Locate every parasitized red blood cell.
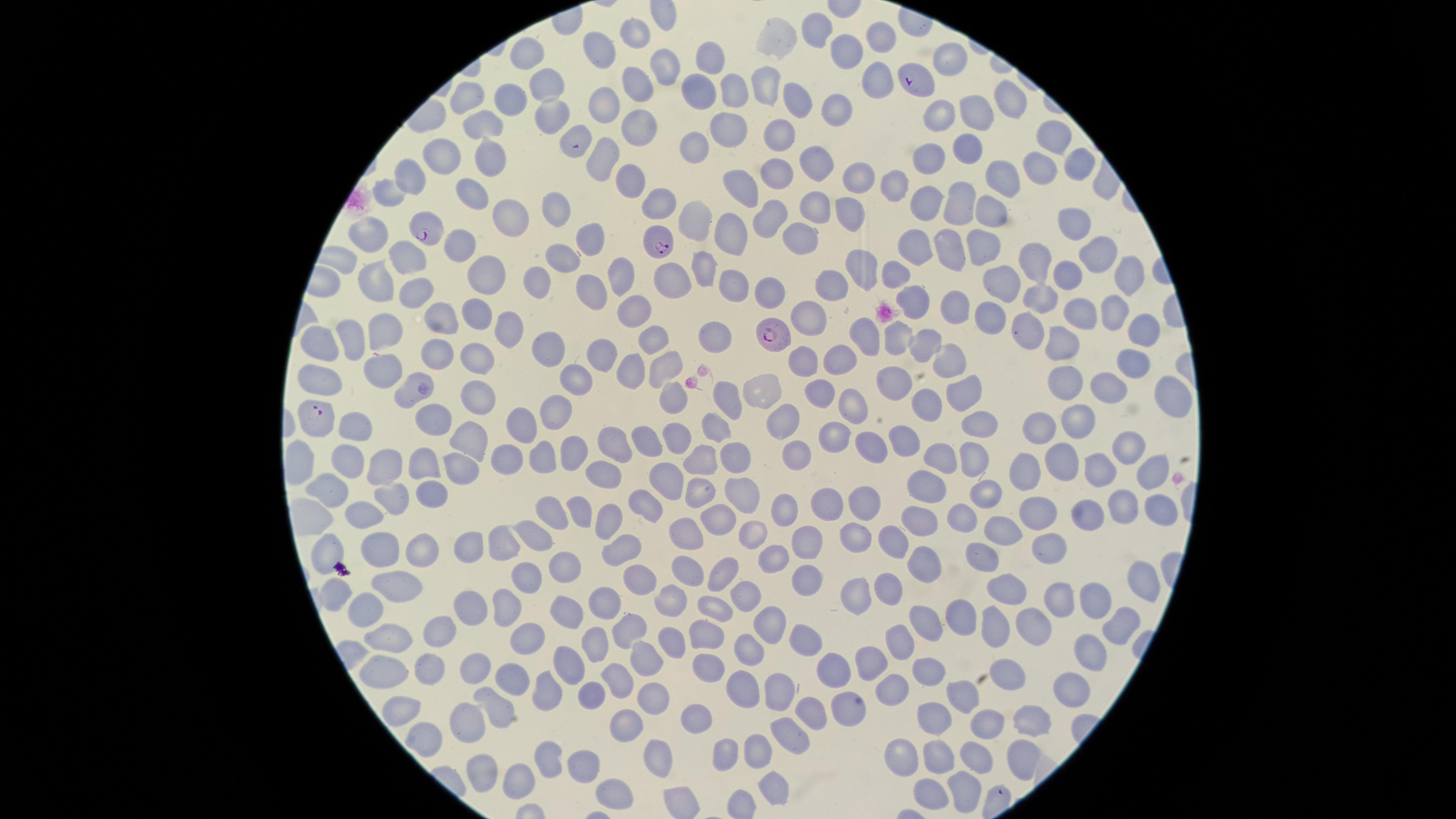

Approximate marker points as {x, y} in pixels.
Parasitized red blood cells: {914, 81}, {426, 230}, {662, 242}, {776, 335}, {314, 416}.

{
  "species": "Plasmodium falciparum",
  "uninfected_red_blood_cells": "approximate marker points as {x, y} in pixels: {823, 26}, {641, 33}, {881, 34}, {776, 39}, {848, 49}, {523, 53}, {603, 54}, {952, 57}, {708, 59}, {658, 69}, {874, 75}, {541, 78}, {766, 79}, {633, 85}, {705, 88}, {732, 91}, {467, 97}, {509, 98}, {1002, 100}, {804, 101}, {836, 101}, {606, 104}, {969, 111}, {545, 112}, {938, 114}, {479, 121}, {731, 121}, {634, 122}, {580, 129}, {1054, 133}, {778, 134}, {701, 143}, {442, 149}, {971, 150}, {486, 153}, {603, 155}, {1075, 159}, {931, 160}, {1039, 164}, {823, 166}, {410, 171}, {780, 173}, {1008, 175}, {862, 181}, {628, 182}, {898, 184}, {745, 188}, {387, 193}, {468, 196}, {652, 200}, {925, 200}, {958, 202}, {816, 203}, {985, 205}, {555, 209}, {769, 213}, {845, 213}, {505, 217}, {699, 219}, {1068, 221}, {372, 230}, {734, 231}, {587, 238}, {808, 238}, {460, 243}, {922, 244}, {986, 245}, {1099, 248}, {958, 249}, {1041, 255}, {408, 257}, {561, 257}, {865, 263}, {484, 266}, {705, 266}, {897, 270}, {1063, 272}, {539, 273}, {1122, 273}, {626, 274}, {673, 277}, {372, 278}, {839, 279}, {1005, 280}, {733, 283}, {769, 291}, {414, 293}, {593, 293}, {1041, 297}, {919, 302}, {961, 302}, {1112, 309}, {1085, 310}, {640, 311}, {440, 313}, {471, 314}, {810, 315}, {993, 316}, {499, 325}, {1026, 326}, {1140, 326}, {387, 332}, {351, 334}, {871, 334}, {716, 335}, {897, 337}, {321, 338}, {654, 340}, {929, 340}, {1066, 341}, {475, 352}, {596, 352}, {547, 353}, {837, 355}, {436, 356}, {953, 356}, {1136, 359}, {665, 363}, {376, 371}, {637, 371}, {316, 376}, {580, 376}, {893, 376}, {1066, 379}, {1108, 381}, {758, 386}, {408, 390}, {820, 391}, {967, 391}, {664, 392}, {1177, 392}, {724, 395}, {468, 400}, {924, 401}, {557, 403}, {853, 403}, {984, 416}, {426, 417}, {520, 419}, {781, 420}, {1075, 420}, {1045, 422}, {717, 426}, {361, 428}, {835, 434}, {651, 438}, {910, 439}, {679, 442}, {473, 443}, {865, 443}, {1126, 443}, {610, 445}, {795, 450}, {569, 453}, {732, 455}, {1056, 455}, {539, 457}, {351, 458}, {506, 458}, {948, 458}, {702, 459}, {972, 459}, {385, 465}, {426, 465}, {463, 469}, {1102, 470}, {601, 472}, {1024, 478}, {1146, 478}, {667, 480}, {921, 481}, {322, 485}, {739, 489}, {696, 490}, {983, 494}, {429, 496}, {392, 500}, {860, 500}, {827, 503}, {1126, 506}, {553, 507}, {650, 508}, {791, 508}, {580, 509}, {1038, 513}, {603, 514}, {357, 516}, {924, 518}, {1151, 518}, {1085, 519}, {958, 520}, {713, 522}, {1010, 529}, {749, 531}, {534, 534}, {856, 536}, {682, 539}, {893, 540}, {806, 541}, {1056, 542}, {466, 547}, {497, 547}, {381, 548}, {628, 549}, {420, 550}, {988, 554}, {326, 556}, {768, 558}, {921, 560}, {566, 564}, {683, 567}, {726, 569}, {534, 572}, {804, 577}, {1137, 579}, {637, 582}, {396, 584}, {331, 587}, {892, 587}, {1003, 592}, {741, 593}, {1096, 595}, {859, 596}, {1059, 600}, {465, 602}, {566, 602}, {506, 604}, {670, 604}, {370, 606}, {605, 606}, {709, 606}, {960, 619}, {924, 623}, {770, 625}, {992, 625}, {1025, 627}, {526, 629}, {625, 631}, {1117, 632}, {443, 633}, {707, 634}, {396, 636}, {804, 637}, {901, 637}, {675, 643}, {590, 646}, {754, 646}, {1086, 649}, {651, 656}, {869, 658}, {482, 664}, {832, 668}, {707, 669}, {925, 669}, {435, 670}, {563, 670}, {380, 674}, {1017, 675}, {509, 678}, {619, 680}, {741, 685}, {1071, 685}, {889, 687}, {770, 688}, {545, 689}, {594, 691}, {654, 696}, {970, 696}, {497, 706}, {839, 706}, {404, 707}, {808, 713}, {696, 715}, {938, 715}, {1027, 715}, {470, 721}, {984, 721}, {627, 725}, {789, 733}, {424, 739}, {756, 749}, {659, 751}, {722, 752}, {904, 755}, {549, 756}, {933, 759}, {978, 760}, {480, 761}, {1021, 761}, {589, 762}, {523, 775}, {762, 783}, {617, 790}, {933, 793}, {962, 793}",
  "visible_region": "circular",
  "image_size": "1456×819 pixels",
  "field_of_view": "single",
  "stain": "Giemsa",
  "capture": "smartphone photograph through the microscope eyepiece",
  "preparation": "thin smear of blood"
}